Comment on the morphology of the red blood cells.
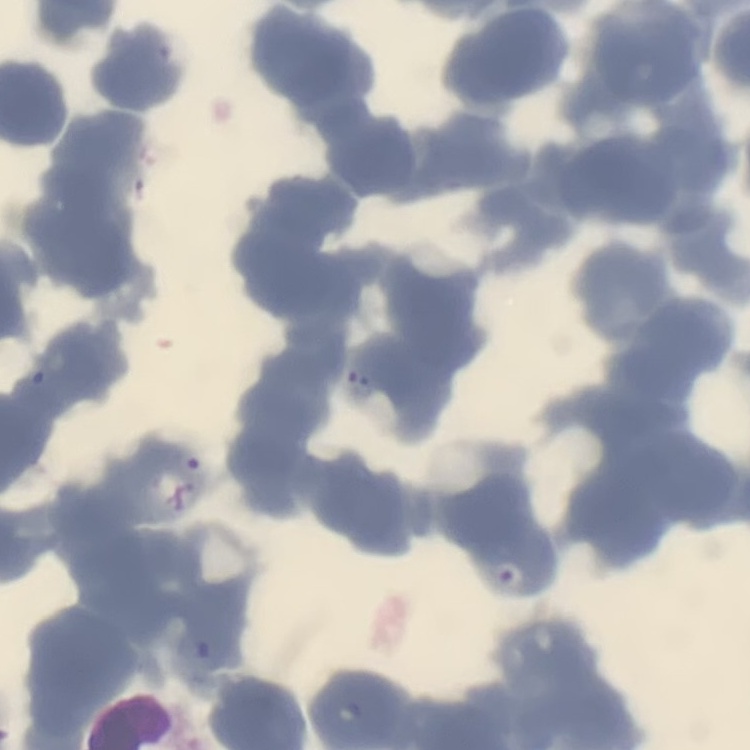

Rouleaux formation.

preparation: thin blood smear
stain: Field's or Giemsa
image_type: square crop of a larger photomicrograph